Assess this cell for malaria.
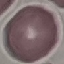
Uninfected.

Cell patch, automatically extracted from a larger field of view and resized to 64 × 64 pixels. Photographed with a smartphone camera at the microscope eyepiece. Giemsa-stained preparation. Thin blood film.